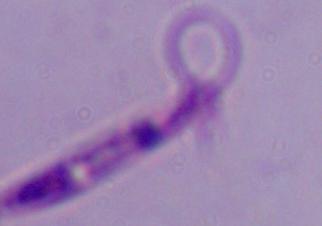

modality: photomicrograph
identification: Leishmania
magnification: 1000x